Describe the morphology of the red blood cells.
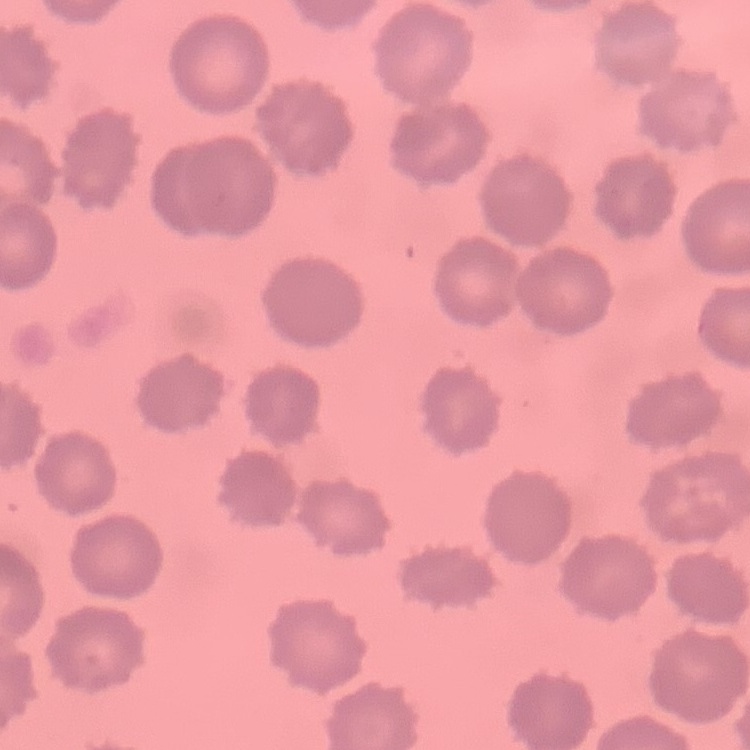
No rouleaux formation.

Thin peripheral smear. Field's or Giemsa stain. One tile cut from a larger photomicrograph.